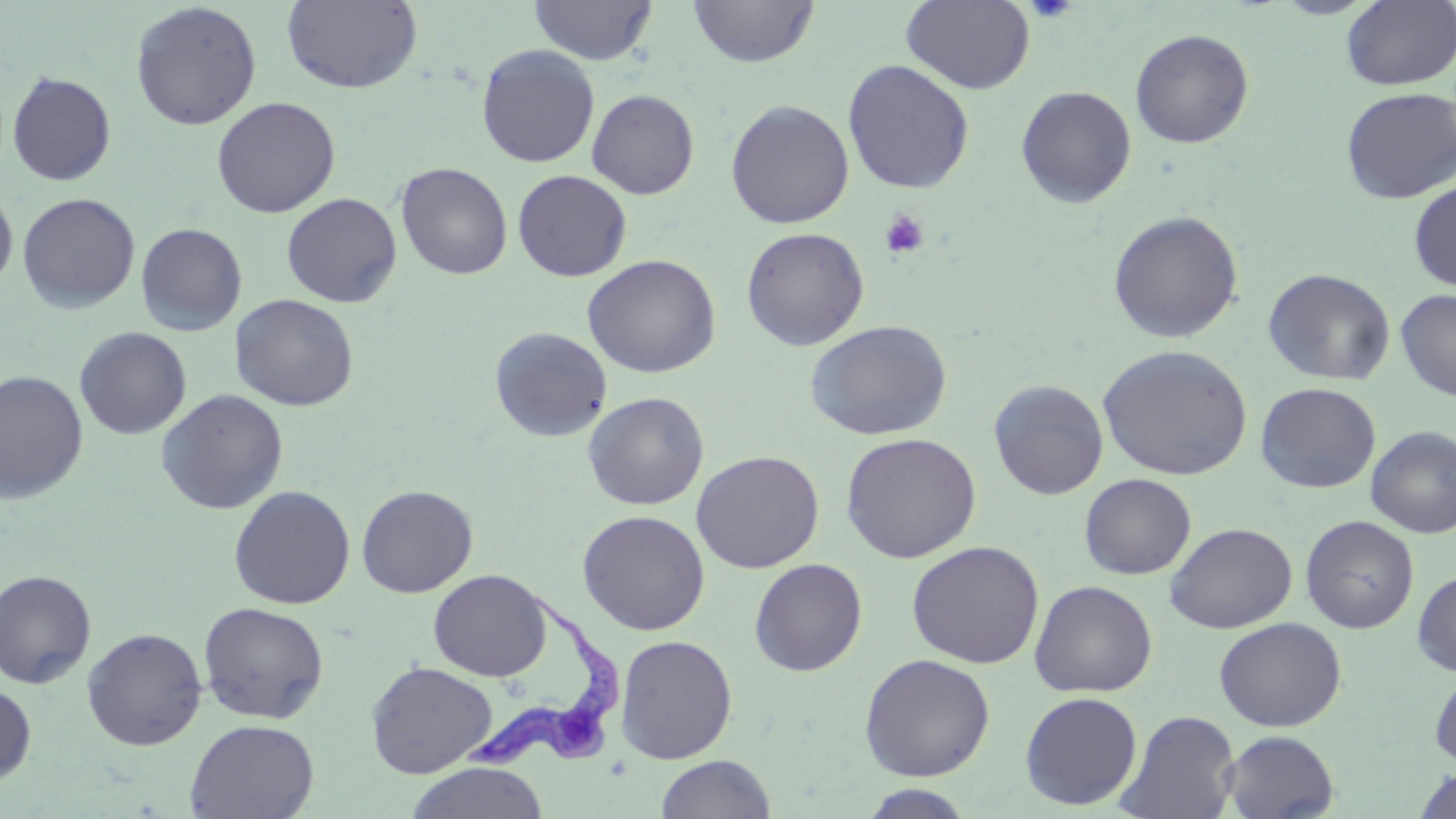 Approximate bounding boxes as (x1,y1)-(x2,y2) corner pairs in pixels. Uninfected red blood cell locations: (281,0)-(424,94), (528,0)-(657,66), (902,0)-(1035,94), (687,1)-(819,68), (1341,1)-(1455,90), (130,2)-(262,131), (1130,28)-(1254,149), (476,44)-(600,167), (842,59)-(975,194), (6,71)-(116,185), (1016,85)-(1137,208), (1340,86)-(1455,204), (586,89)-(699,200), (211,97)-(340,218), (725,99)-(854,229), (395,161)-(513,280), (512,169)-(632,282), (1409,179)-(1456,292), (0,187)-(17,293), (17,192)-(140,313), (281,192)-(403,307), (1108,210)-(1243,343), (135,222)-(247,336), (741,227)-(869,351), (582,254)-(721,378), (1262,268)-(1396,385), (1395,289)-(1456,401), (230,294)-(359,411), (805,319)-(952,441), (489,326)-(613,442), (74,327)-(192,439), (1097,344)-(1252,481), (0,370)-(88,503), (988,379)-(1108,500), (1255,382)-(1381,494), (155,389)-(289,515), (583,391)-(709,510), (1366,426)-(1456,539), (840,432)-(981,563), (691,449)-(824,573), (1080,473)-(1196,579), (356,484)-(478,598), (228,485)-(356,609), (577,509)-(710,635), (1300,515)-(1419,633), (1164,522)-(1298,634), (907,540)-(1044,668), (749,558)-(868,676), (1413,568)-(1456,676), (0,569)-(97,688), (428,569)-(551,682), (1029,580)-(1157,698), (198,601)-(329,724), (1214,617)-(1346,731), (82,627)-(207,750), (615,634)-(737,763), (859,653)-(995,781), (365,661)-(497,778), (1429,665)-(1456,772), (0,681)-(37,786), (1019,691)-(1143,810), (1117,710)-(1241,819), (185,718)-(319,819), (1221,730)-(1340,818), (655,754)-(776,818), (405,762)-(549,819), (1415,768)-(1456,818), (859,784)-(977,818). Trypanosoma brucei locations: (464,587)-(625,775). Platelet locations: (1026,0)-(1078,22), (880,210)-(929,260). Slide-level diagnosis: Trypanosoma brucei. Image is 1456×819 pixels. Thin blood smear. Captured at 1000x magnification. Single field of view. May-Grünwald-Giemsa-stained preparation. Optical microscopy.